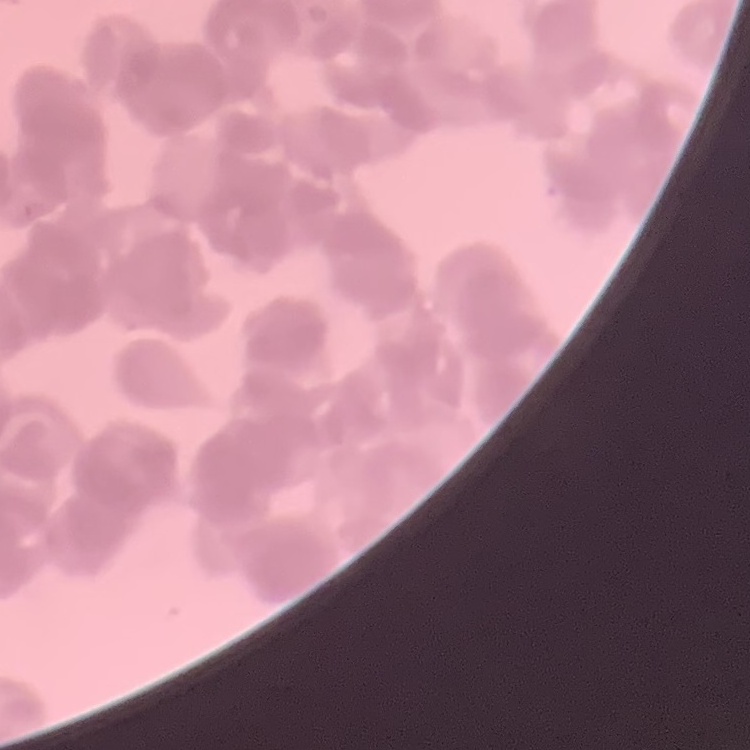

red_blood_cell_morphology: rouleaux formation
stain: Field's or Giemsa
image_type: one tile cut from a larger photomicrograph
preparation: thin peripheral smear